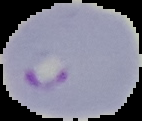
image type = cell region segmented out of the field of view; surrounding area masked to black
result = malaria parasites identified
image size = 142×121 pixels
preparation = thin blood smear